Comment on the morphology of the red blood cells.
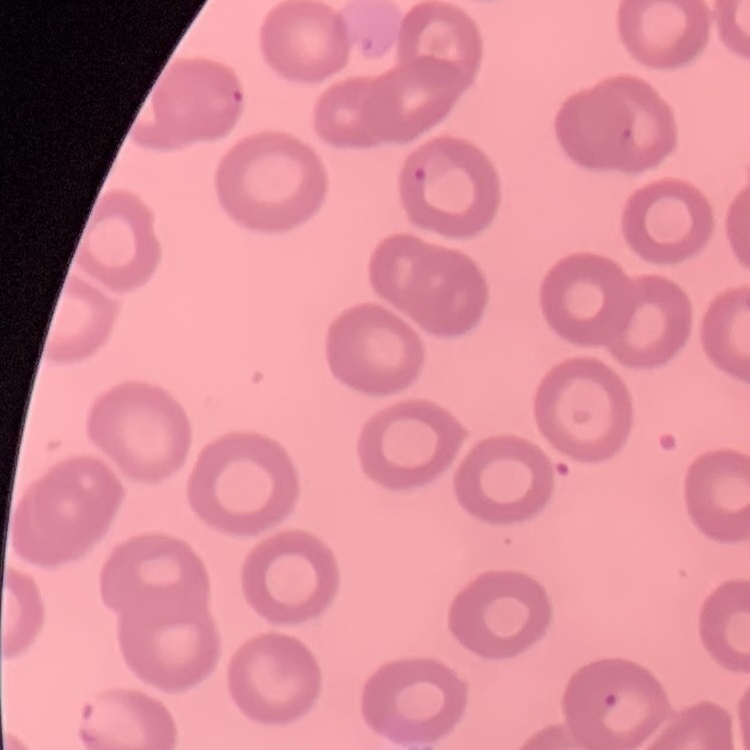
No rouleaux formation.

stain = Field's or Giemsa
image type = one tile cut from a larger photomicrograph
preparation = thin blood film